Assess this cell for malaria.
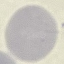

It is uninfected.

Cell patch, automatically extracted from a larger field of view and resized to 64 × 64 pixels. Thin smear of blood. Giemsa-stained preparation. Photographed with a smartphone camera at the microscope eyepiece.